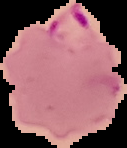
preparation: thin blood film
image_type: segmented cell region on a black background
malaria_status: parasitized
image_size: 127×148 pixels